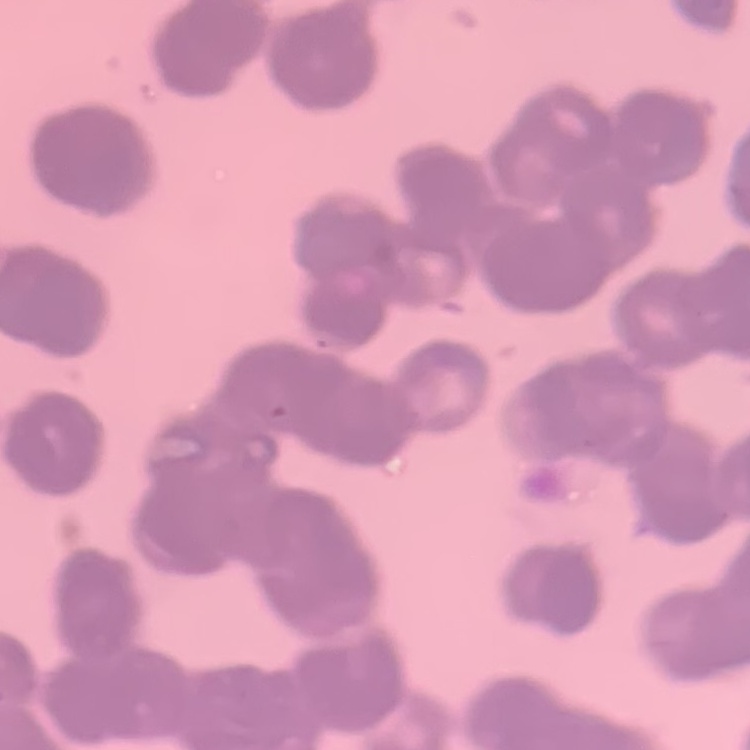 The red blood cells exhibit rouleaux formation. Square crop of a larger photomicrograph. Stained with either Field's or Giemsa. Thin blood film.